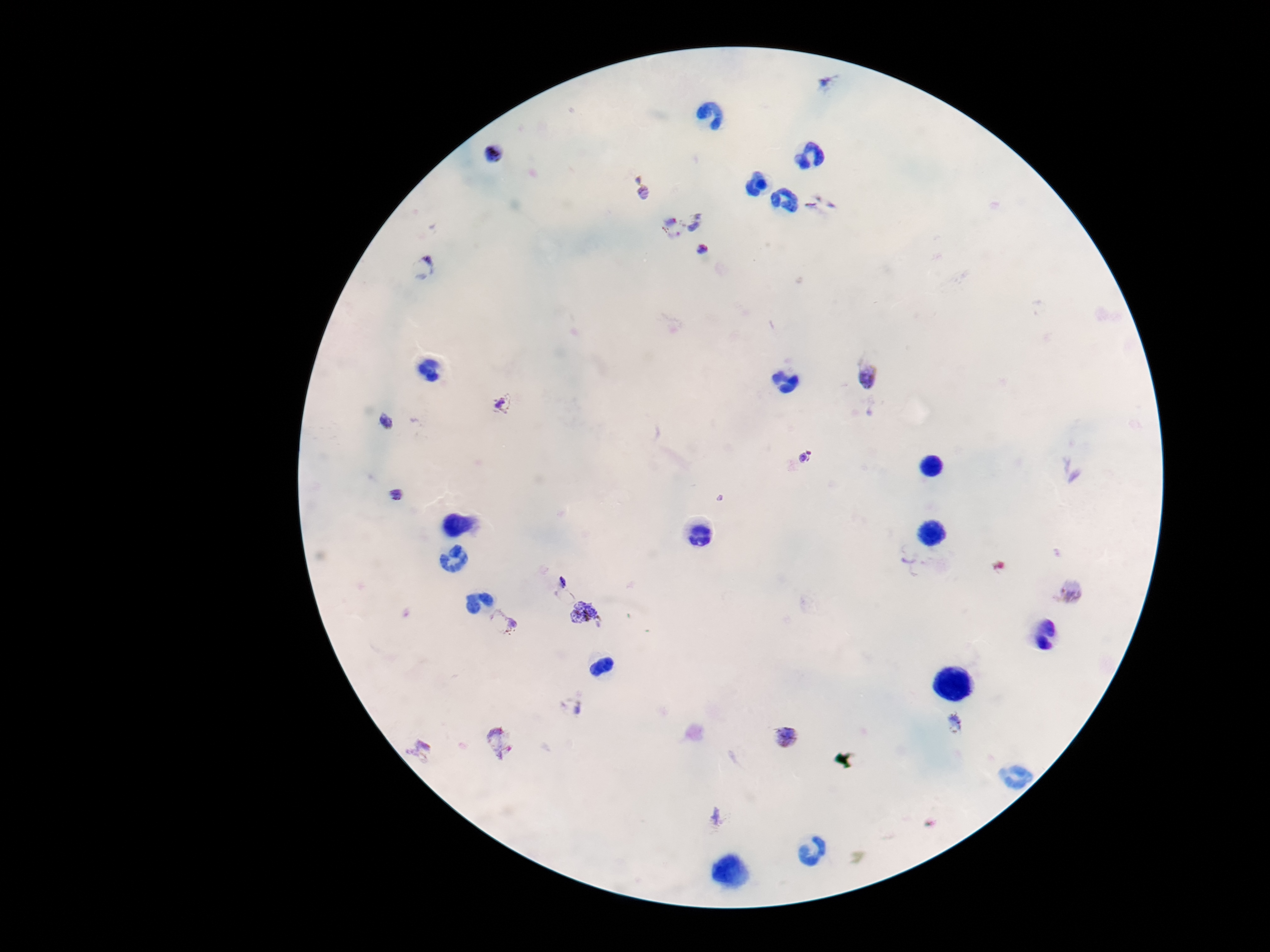
field of view = one from this slide
image size = 1270×952 pixels
Plasmodium parasite locations = approximate object centers, in pixels from the top-left corner: (x=831, y=82), (x=495, y=153), (x=641, y=189), (x=695, y=219), (x=669, y=230), (x=704, y=250), (x=423, y=267), (x=868, y=375), (x=504, y=403), (x=385, y=422), (x=809, y=457), (x=396, y=496), (x=556, y=582), (x=1070, y=591), (x=586, y=613), (x=501, y=620), (x=572, y=706), (x=955, y=723), (x=787, y=736), (x=497, y=741), (x=420, y=750), (x=719, y=817)
magnification = 100x
patient malaria status = infected
preparation = thick blood film
stain = Giemsa
capture = smartphone camera through the microscope eyepiece